Classify this cell by malaria status.
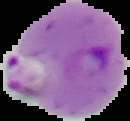
Parasitized.

Summary:
  - Image type: segmented cell region with the area outside set to black
  - Image size: 130×121 pixels
  - Preparation: thin blood film